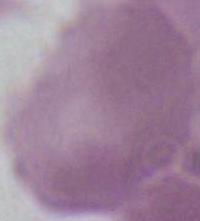

Summary:
  - Modality: micrograph
  - Identification: erythrocyte
  - Magnification: 1000x